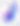

{
  "modality": "micrograph",
  "magnification": "400x",
  "identification": "Toxoplasma gondii"
}